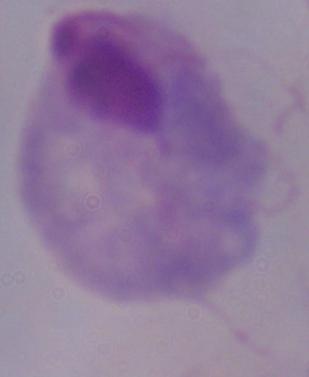

1000x magnification. A trichomonad is shown. Photomicrograph.